Point out every malaria parasite and every leukocyte.
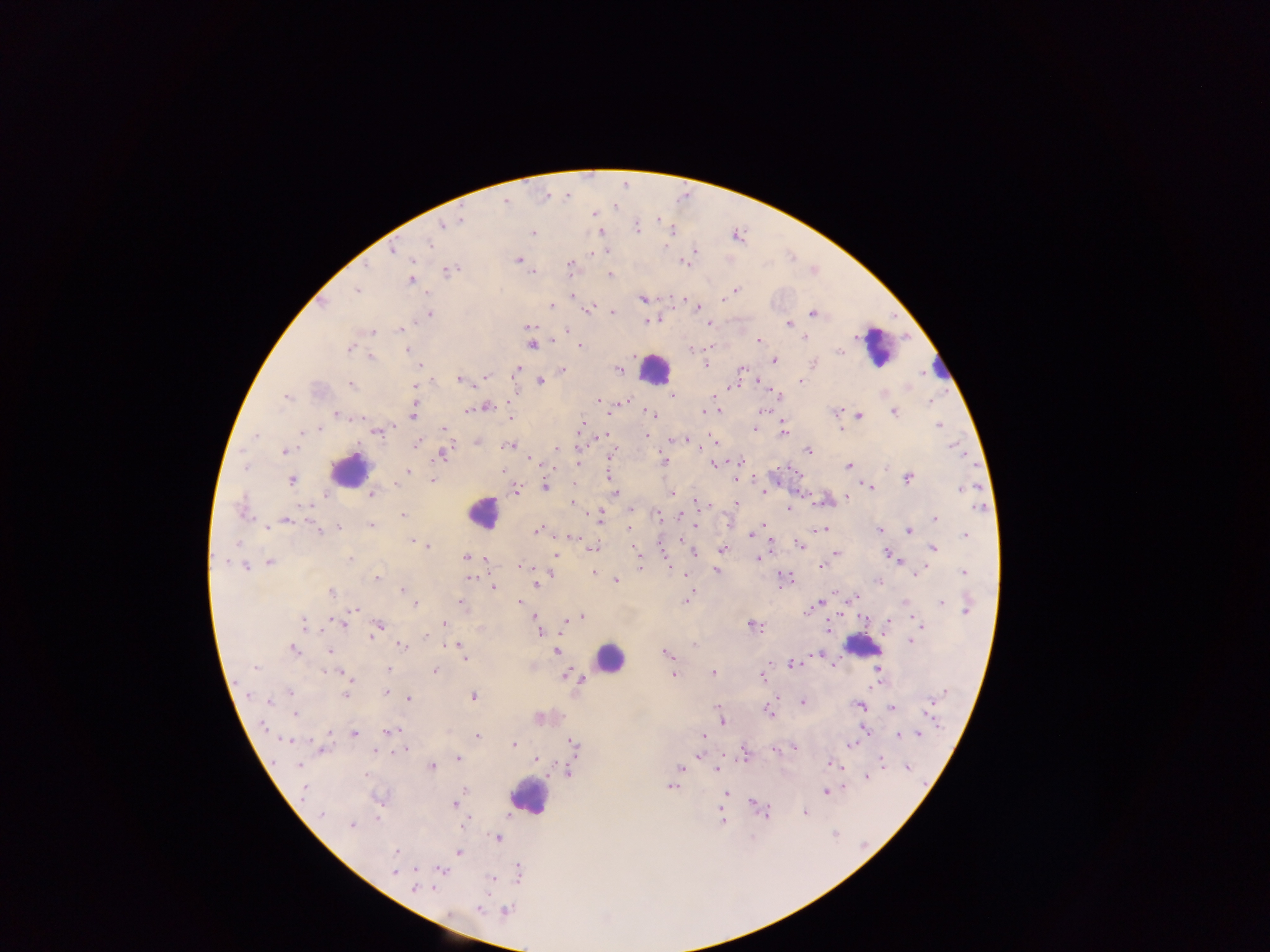

Approximate centers as (x, y) in pixels.
Malaria parasites: (567, 194), (544, 197), (506, 202), (616, 208), (594, 211), (592, 215), (459, 218), (658, 220), (442, 226), (638, 230), (671, 232), (532, 233), (599, 233), (429, 244), (666, 248), (606, 250), (695, 250), (393, 251), (593, 252), (517, 259), (410, 262), (570, 265), (683, 265), (368, 268), (448, 271), (534, 274), (610, 275), (410, 280), (737, 290), (356, 291), (574, 295), (641, 298), (683, 299), (687, 299), (721, 299), (695, 304), (325, 306), (551, 306), (589, 309), (430, 312), (612, 312), (814, 315), (646, 321), (709, 324), (788, 324), (528, 325), (400, 329), (567, 330), (372, 332), (854, 337), (804, 339), (907, 339), (758, 341), (532, 345), (580, 345), (351, 347), (837, 352), (774, 360), (813, 363), (704, 364), (418, 365), (517, 369), (617, 369), (743, 369), (563, 370), (924, 374), (457, 379), (799, 380), (540, 382), (759, 384), (910, 385), (353, 386), (415, 387), (671, 394), (597, 401), (626, 401), (929, 402), (487, 406), (466, 409), (701, 409), (717, 410), (763, 410), (894, 411), (652, 413), (338, 415), (860, 416), (411, 417), (510, 417), (939, 424), (319, 428), (841, 429), (754, 430), (374, 431), (300, 433), (784, 433), (605, 435), (646, 436), (712, 438), (477, 442), (687, 442), (418, 443), (695, 445), (507, 446), (560, 448), (953, 449), (283, 451), (808, 451), (614, 452), (443, 454), (530, 459), (662, 459), (537, 462), (662, 463), (739, 463), (576, 465), (713, 465), (849, 465), (409, 472), (608, 478), (908, 478), (291, 480), (432, 480), (736, 482), (869, 485), (544, 486), (396, 487), (872, 488), (960, 488), (516, 490), (671, 493), (766, 493), (371, 496), (846, 496), (574, 503), (701, 503), (735, 503), (304, 506), (978, 508), (241, 509), (789, 510), (657, 514), (401, 515), (598, 517), (679, 517), (933, 519), (289, 520), (370, 525), (765, 525), (628, 526), (823, 527), (337, 528), (695, 528), (878, 528), (537, 529), (266, 530), (909, 532), (752, 534), (748, 535), (965, 536), (573, 538), (412, 539), (237, 542), (419, 542), (801, 546), (428, 547), (934, 548), (593, 549), (635, 549), (721, 549), (662, 550), (694, 552), (836, 552), (886, 552), (559, 554), (466, 557), (556, 557), (351, 558), (757, 559), (223, 562), (899, 562), (270, 563), (246, 565), (639, 566), (822, 567), (520, 568), (716, 570), (594, 572), (963, 572), (784, 575), (917, 575), (377, 576), (472, 577), (616, 580), (535, 581), (879, 583), (494, 588), (400, 590), (332, 592), (855, 597), (688, 598), (460, 600), (941, 601), (520, 602), (818, 602), (906, 603), (417, 605), (354, 609), (809, 612), (966, 612), (583, 615), (536, 616), (913, 619), (305, 621), (565, 622), (445, 624), (922, 624), (306, 625), (341, 625), (751, 625), (758, 625), (380, 626), (828, 628), (923, 630), (540, 631), (369, 638), (424, 638), (909, 641), (452, 644), (400, 646), (458, 646), (292, 651), (330, 651), (558, 651), (667, 654), (818, 654), (465, 660), (791, 664), (256, 668), (389, 669), (878, 669), (433, 670), (713, 672), (329, 673), (672, 674), (575, 675), (349, 677), (872, 684), (289, 692), (385, 693), (345, 695), (249, 696), (472, 696), (408, 698), (934, 700), (803, 701), (269, 702), (860, 706), (892, 709), (295, 713), (770, 715), (721, 720), (862, 725), (943, 725), (264, 726), (390, 732), (896, 732), (328, 733), (354, 733), (384, 734), (479, 734), (918, 734), (700, 735), (898, 735), (286, 741), (513, 743), (849, 745), (794, 747), (573, 748), (405, 750), (324, 752), (697, 753), (457, 758), (535, 759), (882, 761), (830, 763), (720, 765), (297, 766), (680, 766), (432, 767), (715, 768), (841, 768), (911, 768), (867, 775), (670, 787), (845, 788), (463, 790), (826, 792), (453, 803), (805, 812), (320, 815), (464, 824), (351, 826), (497, 837), (395, 851), (458, 852), (416, 870), (442, 870), (391, 872), (419, 888), (432, 889), (478, 910).
Leukocytes: (873, 350), (652, 370), (348, 470), (484, 509), (863, 646), (607, 660), (532, 801).

Summary:
  - Preparation: thick blood smear
  - Capture: mobile-phone photograph through a microscope
  - Field of view: single
  - Image size: 1270×952 pixels
  - Country: Ghana